Locate every blood parasite and identify its species.
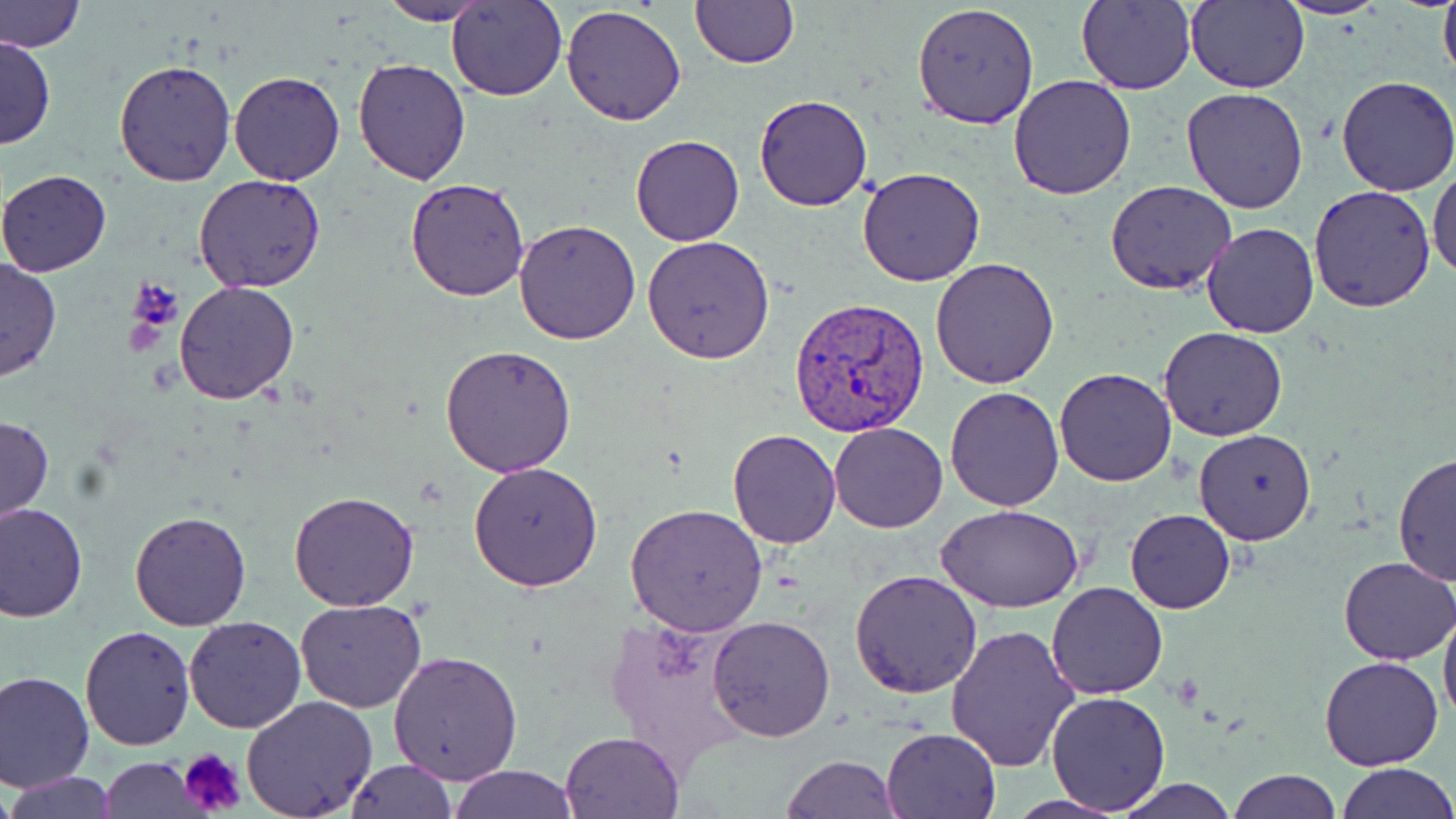

Approximate bounding boxes as (x1, y1, x2, y2) in pixels.
Plasmodium vivax-infected red blood cells: (788, 295, 929, 440).
No Plasmodium falciparum, Plasmodium ovale, Plasmodium malariae, Babesia divergens, or Trypanosoma brucei observed.

Platelet locations: (125, 278, 182, 337), (179, 749, 248, 817). Uninfected red blood cell locations: (1, 0, 84, 53), (377, 0, 491, 24), (446, 0, 566, 101), (1076, 0, 1195, 93), (1275, 0, 1388, 20), (1440, 0, 1456, 86), (689, 1, 799, 68), (1186, 1, 1309, 93), (912, 4, 1040, 129), (562, 5, 687, 127), (0, 35, 55, 151), (352, 59, 472, 184), (114, 62, 236, 186), (229, 71, 344, 185), (1336, 73, 1456, 198), (1008, 74, 1136, 201), (1181, 86, 1310, 213), (753, 93, 873, 211), (630, 135, 744, 246), (1429, 163, 1456, 283), (856, 167, 985, 286), (0, 170, 111, 277), (193, 174, 326, 294), (404, 177, 531, 301), (1105, 181, 1238, 295), (1308, 186, 1436, 312), (514, 218, 642, 345), (1202, 221, 1320, 339), (642, 236, 775, 362), (0, 257, 61, 383), (931, 259, 1061, 389), (173, 279, 302, 405), (1159, 326, 1288, 440), (440, 345, 577, 479), (1054, 367, 1177, 487), (944, 386, 1063, 511), (0, 413, 53, 527), (827, 421, 949, 533), (727, 428, 843, 548), (1194, 428, 1319, 546), (1392, 450, 1456, 589), (468, 462, 603, 591), (289, 490, 419, 611), (0, 502, 87, 620), (624, 504, 769, 635), (936, 505, 1086, 614), (1125, 509, 1235, 615), (129, 510, 252, 629), (1338, 556, 1455, 665), (850, 570, 983, 698), (1047, 582, 1166, 698), (294, 600, 427, 714), (1439, 604, 1456, 731), (708, 614, 835, 740), (606, 615, 759, 776), (184, 616, 309, 734), (945, 621, 1079, 771), (78, 626, 197, 750), (388, 650, 522, 785), (1318, 657, 1444, 772), (0, 670, 94, 790), (1044, 690, 1171, 812), (240, 695, 378, 818), (881, 727, 1002, 818), (560, 729, 685, 819), (782, 754, 902, 818), (100, 757, 212, 818), (347, 760, 456, 818), (1337, 761, 1453, 819), (449, 766, 580, 819), (1228, 770, 1340, 819), (5, 772, 118, 819), (1113, 778, 1238, 818). Slide-level diagnosis: Plasmodium vivax. Image is 1456×819 pixels. Thin blood film. Light microscopy. 1000x magnification. One field of a larger specimen. May-Grünwald-Giemsa stain.